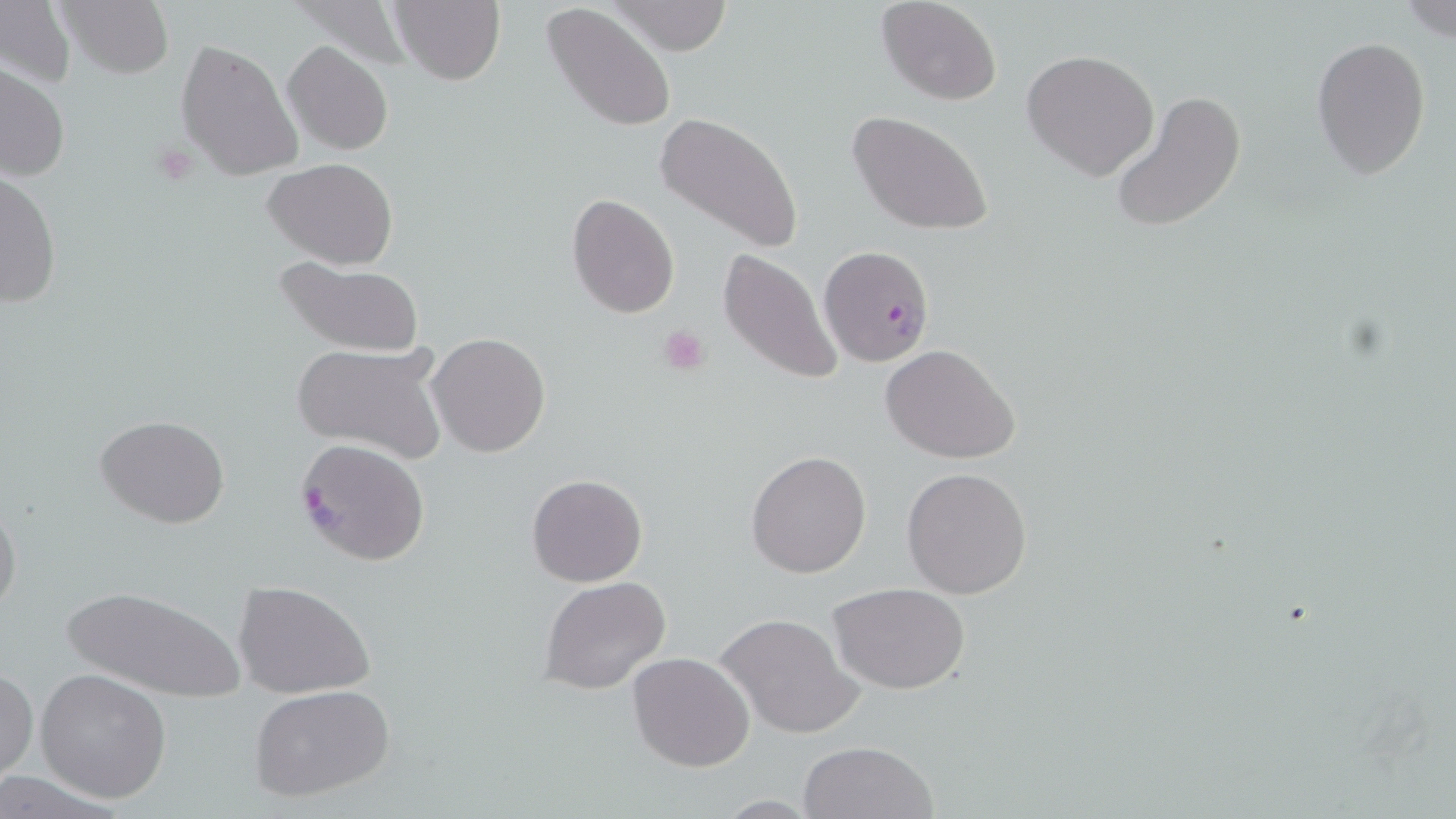

Summary:
  - Coordinate format: approximate bounding boxes as (x1,y1)-(x2,y2) corner pairs in pixels
  - Plasmodium falciparum-infected red blood cell locations: (819,245)-(935,366), (294,438)-(430,567)
  - Platelet locations: (151,142)-(200,185), (657,324)-(713,377)
  - Uninfected red blood cell locations: (0,0)-(75,90), (59,0)-(174,79), (610,0)-(734,55), (875,0)-(1003,105), (390,1)-(506,86), (1400,2)-(1456,42), (541,4)-(676,132), (1312,35)-(1431,183), (176,38)-(304,184), (282,41)-(393,154), (1021,50)-(1160,179), (0,62)-(69,183), (1108,89)-(1247,236), (654,110)-(805,256), (846,110)-(995,236), (263,157)-(399,269), (2,168)-(63,310), (568,193)-(680,320), (718,247)-(844,388), (272,256)-(424,358), (428,333)-(549,458), (291,340)-(450,465), (881,345)-(1021,464), (96,415)-(229,529), (746,450)-(872,578), (902,466)-(1033,600), (526,474)-(648,588), (0,498)-(23,620), (539,575)-(673,694), (233,580)-(374,699), (60,582)-(245,705), (830,583)-(971,695), (715,612)-(862,740), (626,653)-(755,772), (0,667)-(37,782), (35,668)-(172,802), (248,682)-(398,804), (797,739)-(940,819)
  - Slide-level diagnosis: Plasmodium falciparum
  - Modality: optical microscopy
  - Magnification: 1000x
  - Field of view: one of a larger specimen
  - Stain: May-Grünwald-Giemsa
  - Preparation: thin blood smear
  - Image size: 1456×819 pixels